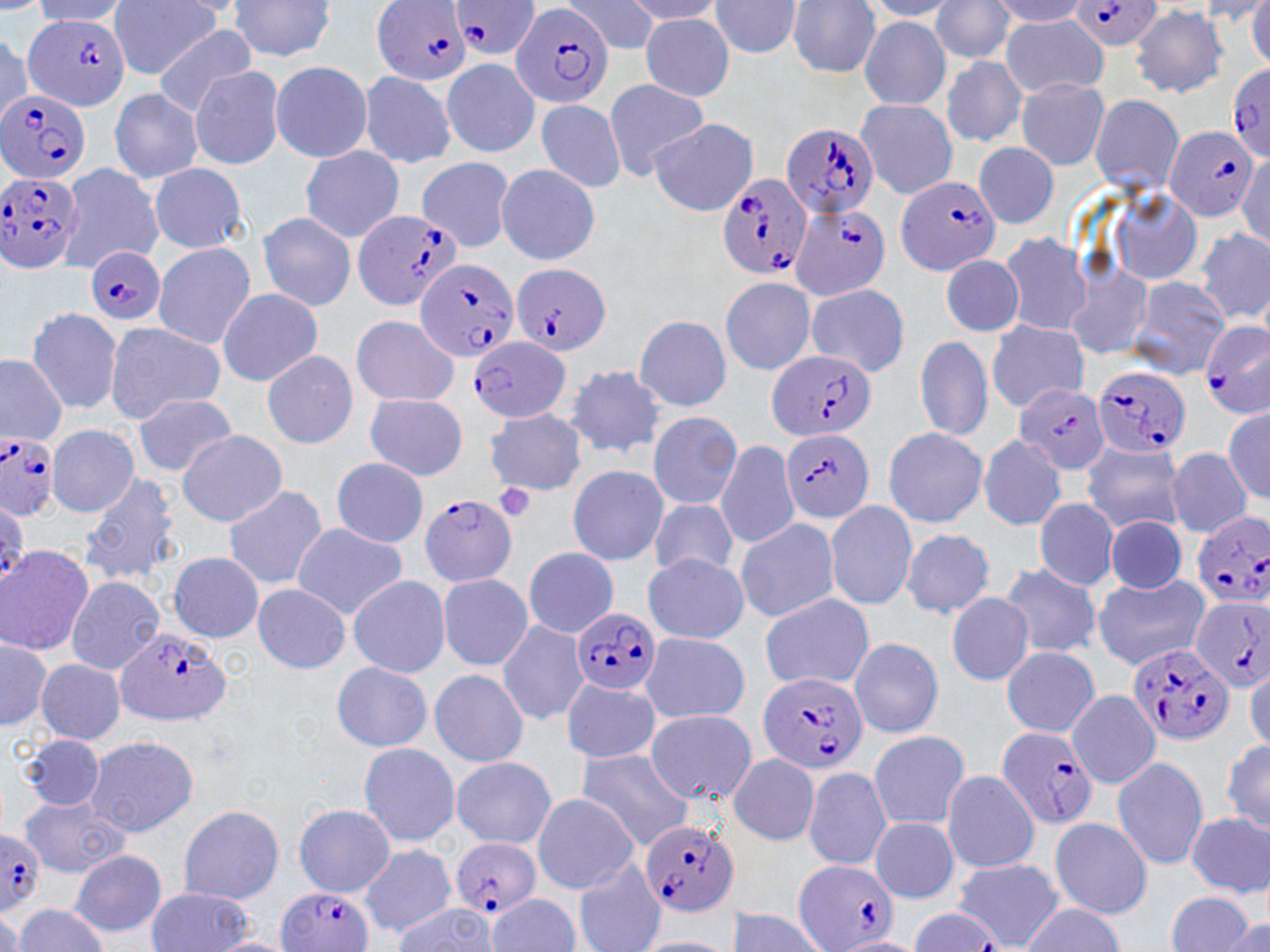

slide-level diagnosis = Plasmodium falciparum
stain = May-Grünwald-Giemsa
modality = light microscopy
preparation = thin blood smear
magnification = 1000x
field of view = one of a larger specimen
uninfected red blood cell locations = approximate bounding boxes as (x1, y1, x2, y2) in pixels: (110, 0, 223, 79), (563, 0, 662, 55), (929, 0, 1015, 63), (988, 0, 1094, 26), (0, 1, 49, 14), (32, 1, 133, 26), (228, 1, 339, 62), (623, 1, 728, 25), (707, 1, 803, 59), (785, 1, 883, 77), (863, 1, 964, 20), (1246, 1, 1269, 70), (1130, 5, 1230, 97), (1000, 13, 1110, 97), (639, 14, 736, 101), (858, 18, 952, 109), (151, 25, 258, 116), (0, 32, 35, 125), (440, 56, 541, 159), (939, 57, 1028, 147), (269, 60, 373, 164), (188, 65, 286, 170), (358, 70, 456, 170), (603, 78, 711, 180), (1016, 78, 1110, 171), (108, 88, 204, 183), (1088, 93, 1184, 197), (534, 98, 626, 194), (854, 99, 958, 200), (648, 118, 759, 217), (974, 141, 1059, 229), (298, 145, 406, 242), (1234, 152, 1268, 249), (417, 156, 515, 252), (494, 162, 601, 265), (148, 163, 248, 254), (60, 164, 163, 272), (1105, 185, 1205, 285), (258, 211, 357, 311), (1196, 227, 1269, 325), (997, 232, 1090, 337), (152, 241, 257, 349), (941, 253, 1025, 337), (1063, 260, 1153, 362), (719, 275, 819, 376), (1126, 275, 1231, 379), (804, 281, 911, 378), (217, 287, 323, 386), (25, 306, 125, 414), (350, 313, 460, 407), (632, 315, 734, 413), (987, 320, 1088, 411), (103, 321, 224, 422), (914, 335, 993, 442), (260, 349, 360, 448), (0, 353, 68, 444), (565, 365, 669, 458), (364, 392, 468, 480), (134, 393, 237, 476), (113, 400, 222, 540), (1221, 405, 1270, 506), (486, 409, 588, 495), (647, 411, 742, 511), (45, 424, 138, 518), (882, 427, 988, 526), (176, 430, 289, 525), (976, 434, 1069, 532), (715, 438, 799, 550), (1080, 439, 1185, 534), (1166, 447, 1252, 538), (330, 457, 430, 547), (566, 464, 669, 565), (80, 470, 182, 588), (221, 484, 327, 590), (648, 497, 739, 579), (1033, 498, 1119, 591), (824, 500, 918, 611), (733, 516, 838, 622), (1104, 517, 1187, 594), (289, 522, 409, 618), (900, 528, 995, 619), (0, 545, 95, 656), (522, 546, 617, 638), (167, 551, 262, 642), (641, 553, 749, 644), (995, 561, 1104, 659), (437, 572, 534, 672), (1094, 573, 1210, 671), (65, 574, 165, 674), (346, 575, 451, 678), (252, 583, 352, 672), (758, 592, 875, 692), (946, 592, 1035, 685), (497, 618, 590, 725), (636, 629, 751, 723), (1, 635, 53, 733), (856, 636, 956, 828), (848, 637, 943, 738), (1001, 646, 1100, 738), (36, 660, 126, 744), (330, 661, 434, 752), (1245, 663, 1270, 752), (430, 668, 529, 769), (561, 677, 661, 765), (1065, 689, 1162, 789), (644, 708, 758, 805), (867, 729, 969, 831), (17, 733, 108, 811), (85, 734, 199, 838), (1219, 736, 1269, 836), (357, 742, 459, 847), (575, 748, 695, 849), (728, 753, 821, 846), (1112, 755, 1208, 872), (451, 756, 557, 848), (801, 766, 892, 870), (941, 770, 1041, 873), (530, 792, 641, 894), (20, 794, 129, 878), (293, 803, 394, 896), (178, 804, 284, 903), (1186, 812, 1269, 897), (869, 815, 959, 902), (1050, 816, 1153, 918), (358, 843, 456, 939), (70, 851, 167, 938), (573, 858, 666, 952), (954, 858, 1063, 949), (145, 887, 257, 952), (1166, 890, 1258, 952), (489, 894, 579, 952), (391, 900, 501, 952), (1022, 902, 1123, 952), (12, 904, 110, 952), (0, 907, 23, 952), (722, 909, 832, 952), (1223, 916, 1270, 952), (831, 935, 926, 951), (208, 936, 295, 951), (631, 936, 740, 952)
Plasmodium falciparum-infected red blood cell locations = approximate bounding boxes as (x1, y1, x2, y2) in pixels: (373, 0, 474, 87), (448, 0, 543, 62), (1073, 0, 1164, 51), (508, 2, 615, 108), (25, 14, 133, 109), (1226, 62, 1270, 162), (0, 89, 92, 184), (782, 123, 880, 218), (1165, 125, 1260, 222), (0, 172, 84, 274), (718, 174, 815, 281), (894, 176, 1003, 277), (790, 204, 892, 302), (351, 210, 462, 312), (84, 246, 166, 326), (415, 258, 519, 364), (511, 262, 612, 358), (1200, 323, 1270, 416), (466, 336, 574, 423), (765, 349, 876, 443), (1093, 366, 1188, 457), (1015, 382, 1109, 475), (779, 427, 874, 523), (0, 433, 59, 519), (421, 493, 517, 587), (1192, 510, 1270, 612), (1191, 598, 1269, 691), (571, 608, 659, 697), (114, 627, 230, 725), (1130, 642, 1235, 747), (756, 669, 869, 774), (995, 725, 1099, 831), (642, 815, 740, 918), (0, 827, 45, 911), (450, 837, 539, 919), (793, 857, 903, 952), (278, 886, 372, 952)
platelet locations = approximate bounding boxes as (x1, y1, x2, y2) in pixels: (492, 483, 536, 525)
image size = 1270×952 pixels